Identify the parasite.
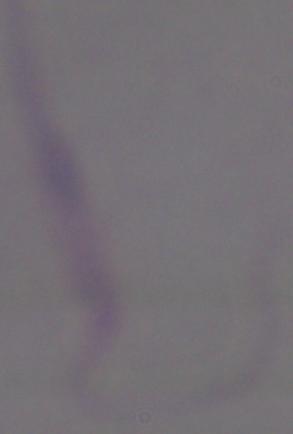

Leishmania.

magnification = 1000x
modality = micrograph